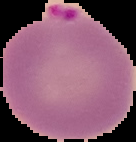

From a thin blood film. The area outside the segmented cell region is set to black. Image is 136×142 pixels. Result: malaria parasites identified.